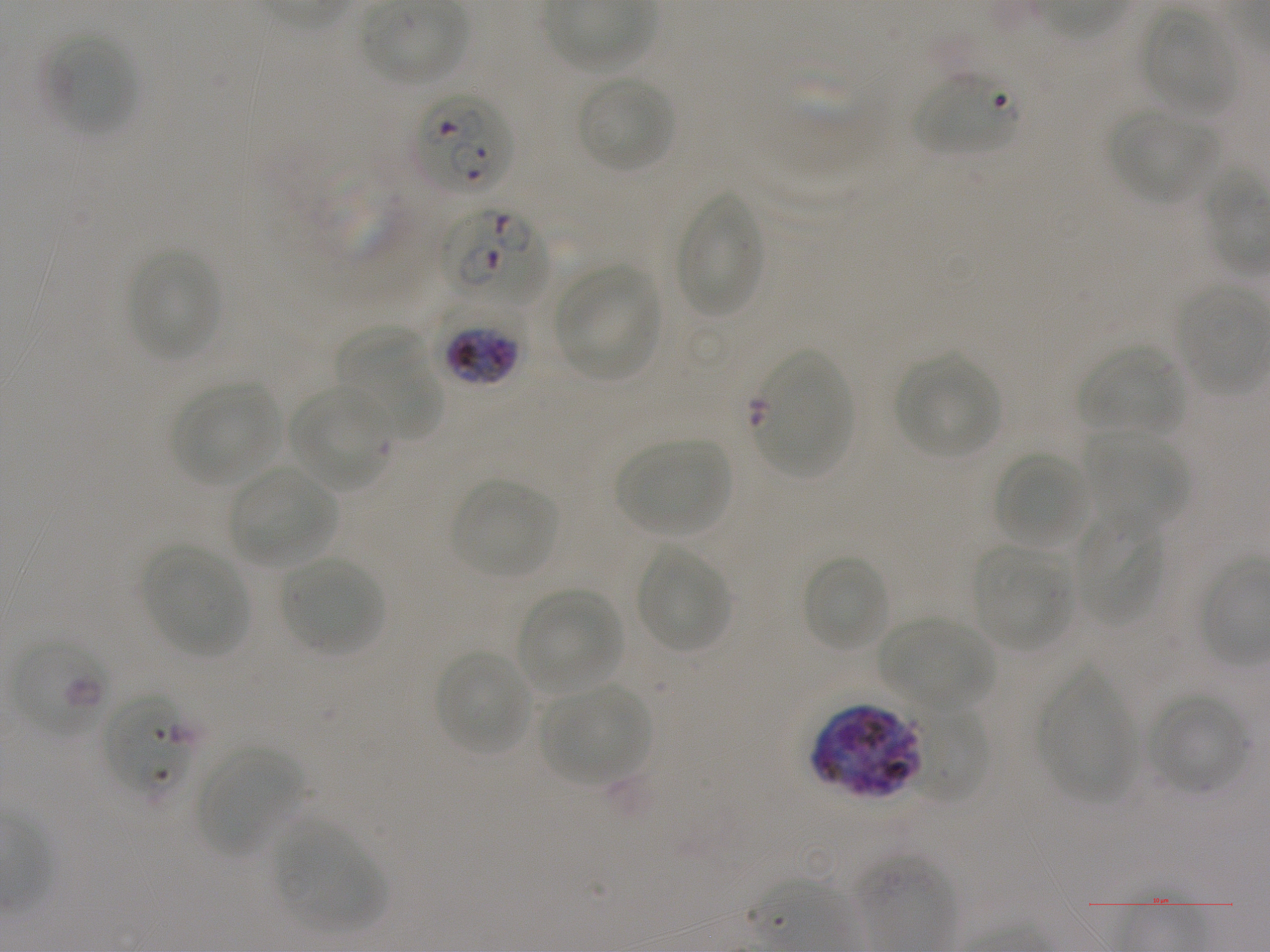

Approximate bounding boxes as [x1, y1, x2, y2] in pixels. Not every red blood cell is marked. A life-cycle stage — or a range of stages, where the recorded stages span more than one — follows each staged infected red blood cell. Locations of uninfected red blood cells: [1141, 11, 1240, 117], [42, 32, 136, 134], [753, 64, 878, 176], [913, 73, 1017, 156], [577, 74, 675, 174], [1112, 111, 1210, 203], [677, 194, 763, 317], [127, 250, 219, 359], [554, 265, 661, 380], [336, 330, 440, 434], [1079, 345, 1186, 437], [894, 354, 1000, 459], [173, 381, 281, 484], [288, 386, 391, 491], [1082, 430, 1187, 528], [616, 437, 733, 537], [994, 451, 1089, 549], [229, 465, 336, 566], [451, 479, 557, 579], [1073, 516, 1163, 625], [971, 545, 1071, 651], [144, 547, 250, 656], [636, 548, 730, 654], [801, 553, 891, 654], [280, 556, 384, 654], [520, 588, 622, 692], [879, 617, 992, 711], [435, 649, 534, 754], [1038, 666, 1138, 803], [540, 685, 649, 785], [1148, 692, 1248, 794], [912, 708, 993, 805], [198, 746, 302, 853], [277, 824, 384, 929], [854, 854, 953, 940]. Locations of red blood cells of indeterminate infection status: [290, 157, 415, 268], [752, 351, 854, 477]. Locations of infected red blood cells: [414, 93, 514, 196]; [443, 207, 548, 306]; [442, 315, 521, 387]; [12, 638, 114, 735] late ring to early trophozoite; [102, 691, 201, 802]; [815, 705, 922, 799]. One field from this slide. Giemsa stain. P. falciparum strain NF54 in static in-vitro culture. Thin blood smear. Blood group of the donor: A+. 100x objective under oil immersion, numerical aperture 1.25. Image is 1270×952 pixels.